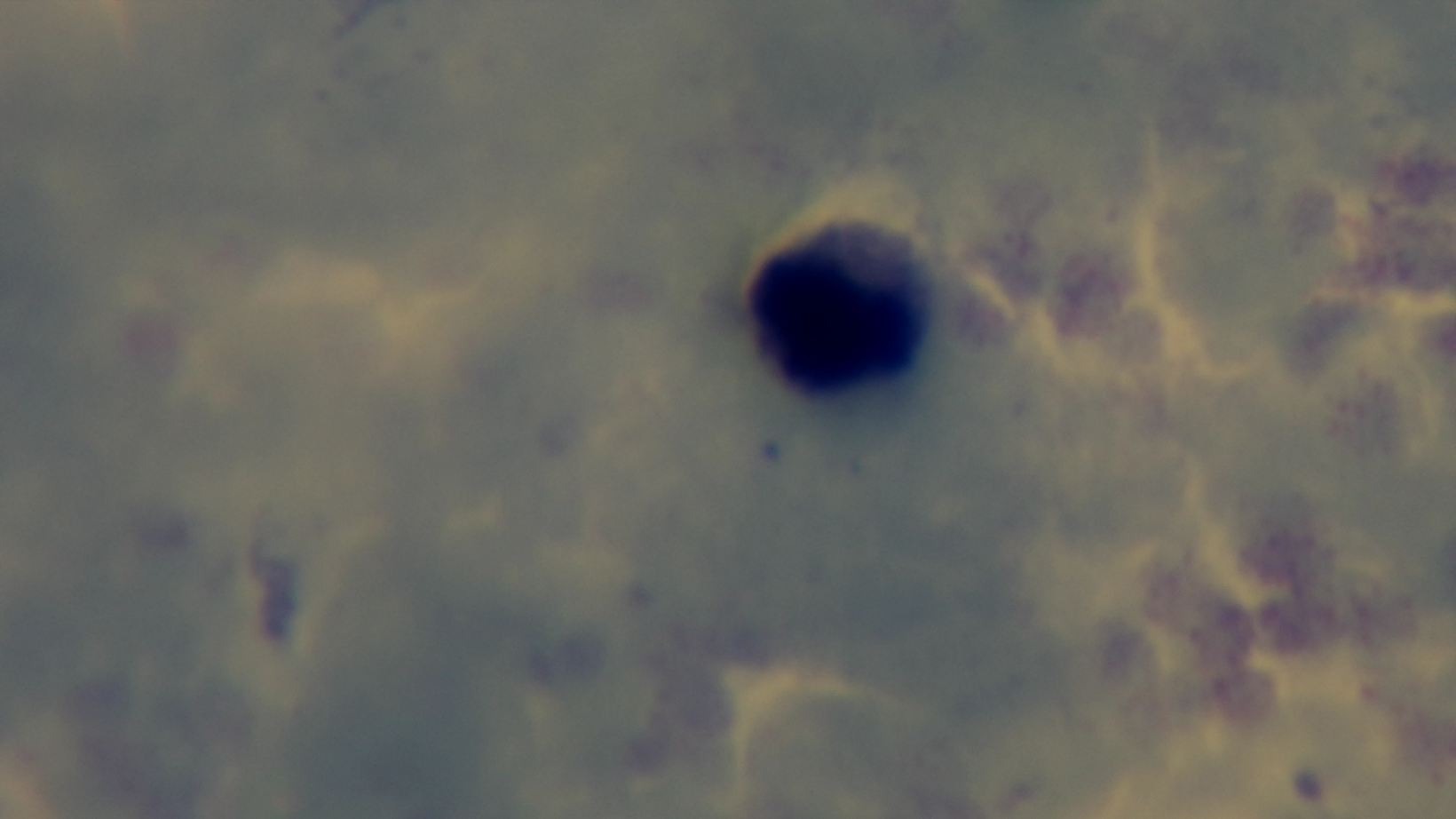
Oil-immersion objective, 100x. Preparation: thick blood film. Photomicrograph. Giemsa stain. Mounted 4K digital camera. Single field of view. Malaria status: negative.